Locate every Plasmodium parasite by life-cycle stage, and every leukocyte.
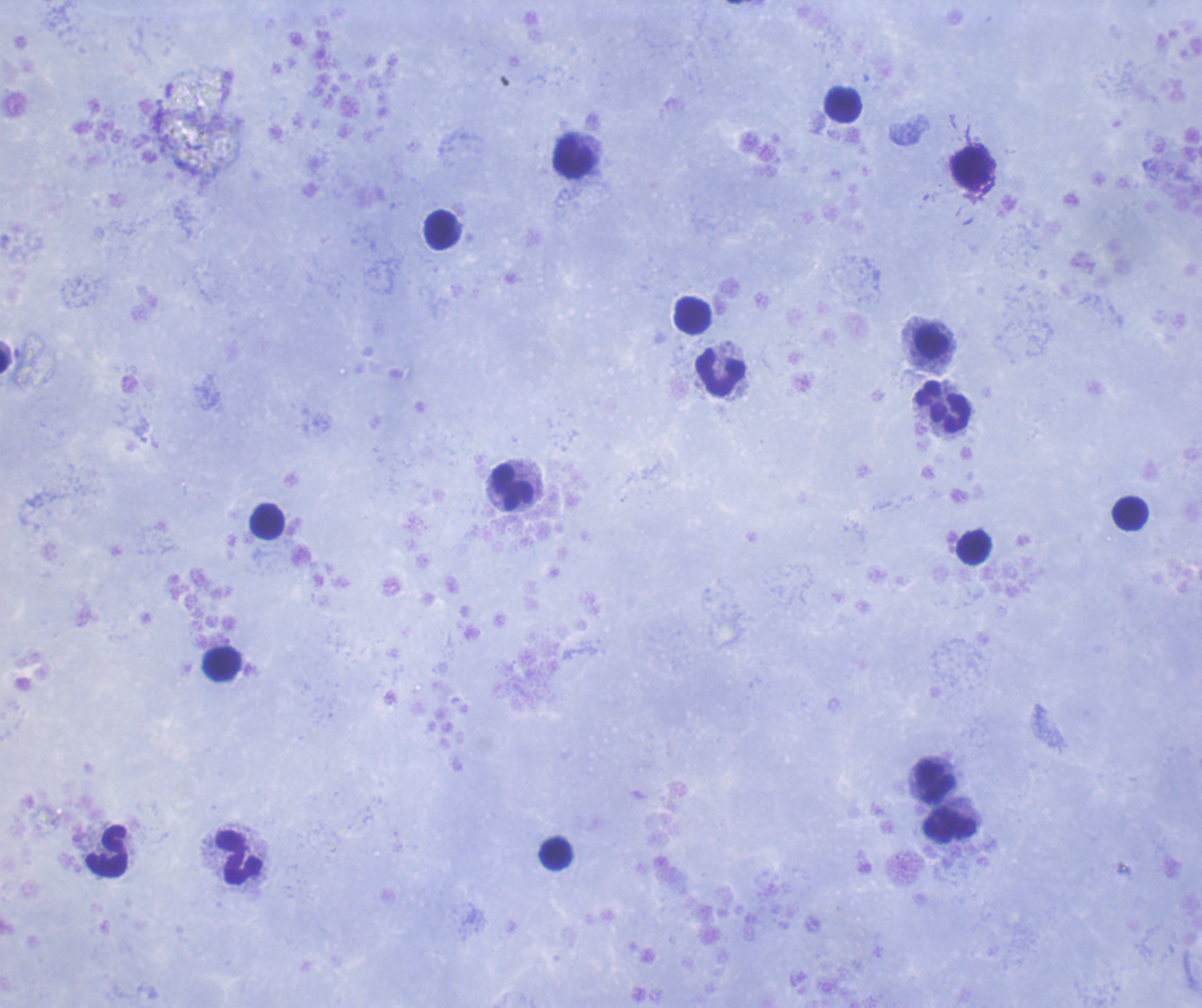
No Plasmodium parasites detected.
Approximate centers as [x, y] in pixels.
Leukocytes: [844, 105], [574, 156], [971, 167], [442, 230], [694, 315], [932, 342], [5, 361], [721, 373], [943, 406], [513, 488], [1130, 513], [267, 522], [974, 547], [221, 664], [936, 782], [950, 825], [105, 852], [555, 854], [239, 857].

Thick smear of blood. Previously used in an actual diagnosis. Background quality: good. Image is 1202×1008 pixels. Coloration quality: good. 100x magnification. Romanowsky-stained preparation. Single field of view.